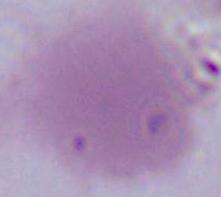

Summary:
  - Magnification: 1000x
  - Modality: micrograph
  - Identification: red blood cell